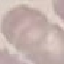

Summary:
  - Malaria status: uninfected
  - Stain: Giemsa
  - Image type: cell patch, automatically extracted from a larger field of view and resized to 64 × 64 pixels
  - Preparation: thin smear
  - Capture: smartphone through the microscope eyepiece